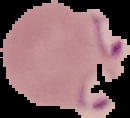
{
  "image_size": "130×118 pixels",
  "image_type": "segmented cell region with the area outside set to black",
  "malaria_status": "parasitized",
  "preparation": "thin blood film"
}